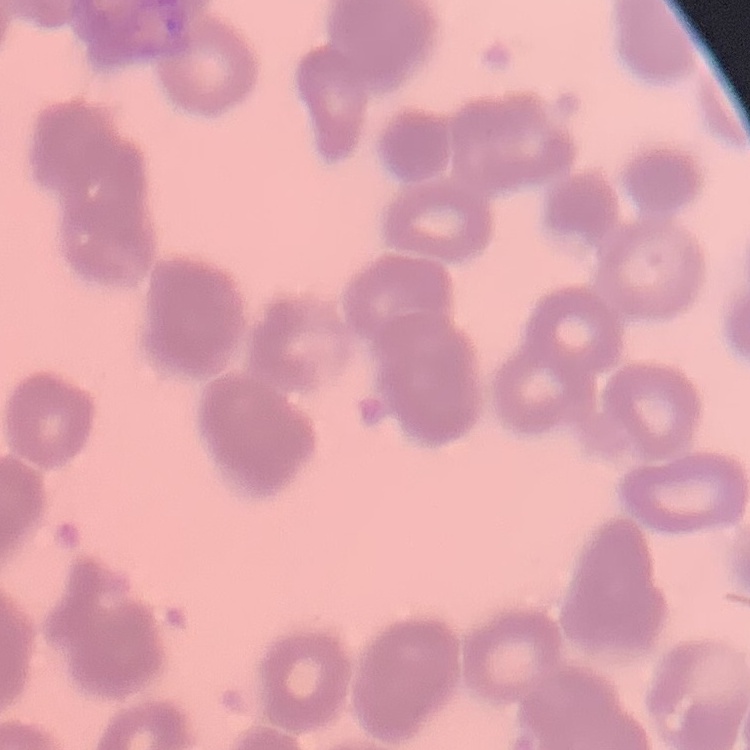

{
  "erythrocyte_morphology": "rouleaux formation",
  "image_type": "square crop of a larger photomicrograph",
  "preparation": "thin blood smear",
  "stain": "Field's or Giemsa"
}